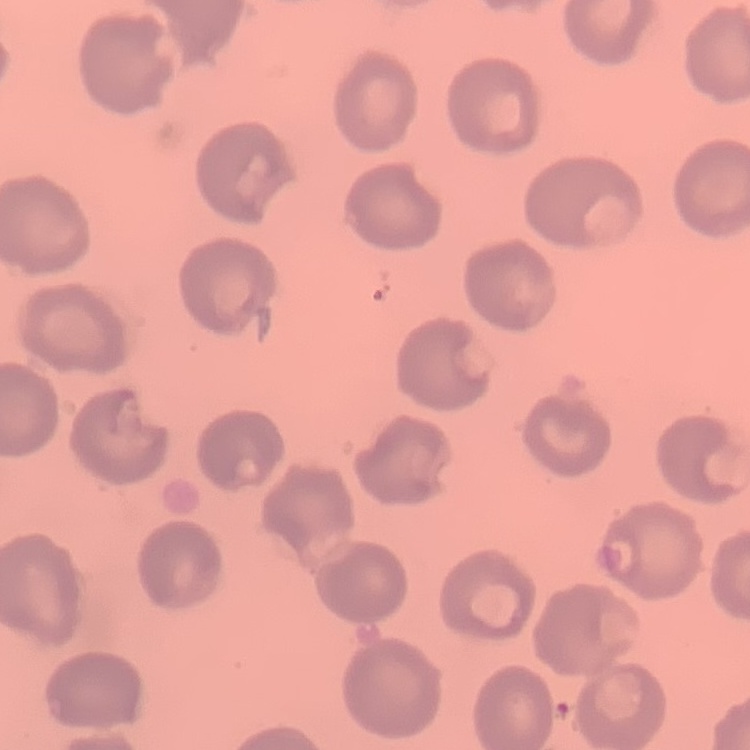 The erythrocytes exhibit no rouleaux formation. Field's or Giemsa stain. Thin blood film. One tile cut from a larger photomicrograph.